Name the parasite shown.
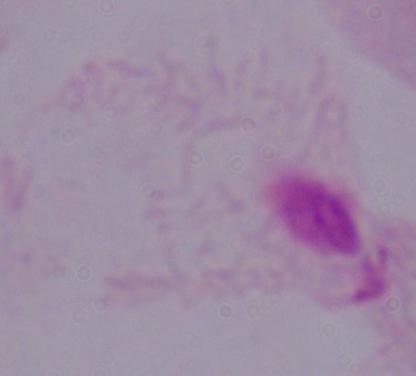

This is a trichomonad.

modality = photomicrograph
magnification = 1000x